Comment on the morphology of the erythrocytes.
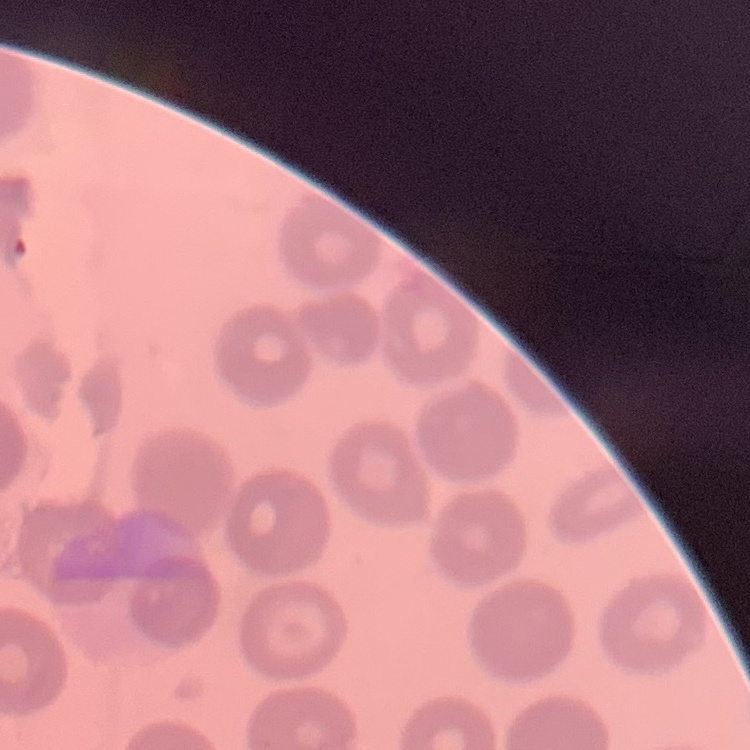
No rouleaux formation.

preparation = thin blood smear
stain = Field's or Giemsa
image type = square crop of a larger photomicrograph